Locate every blood parasite and identify its species.
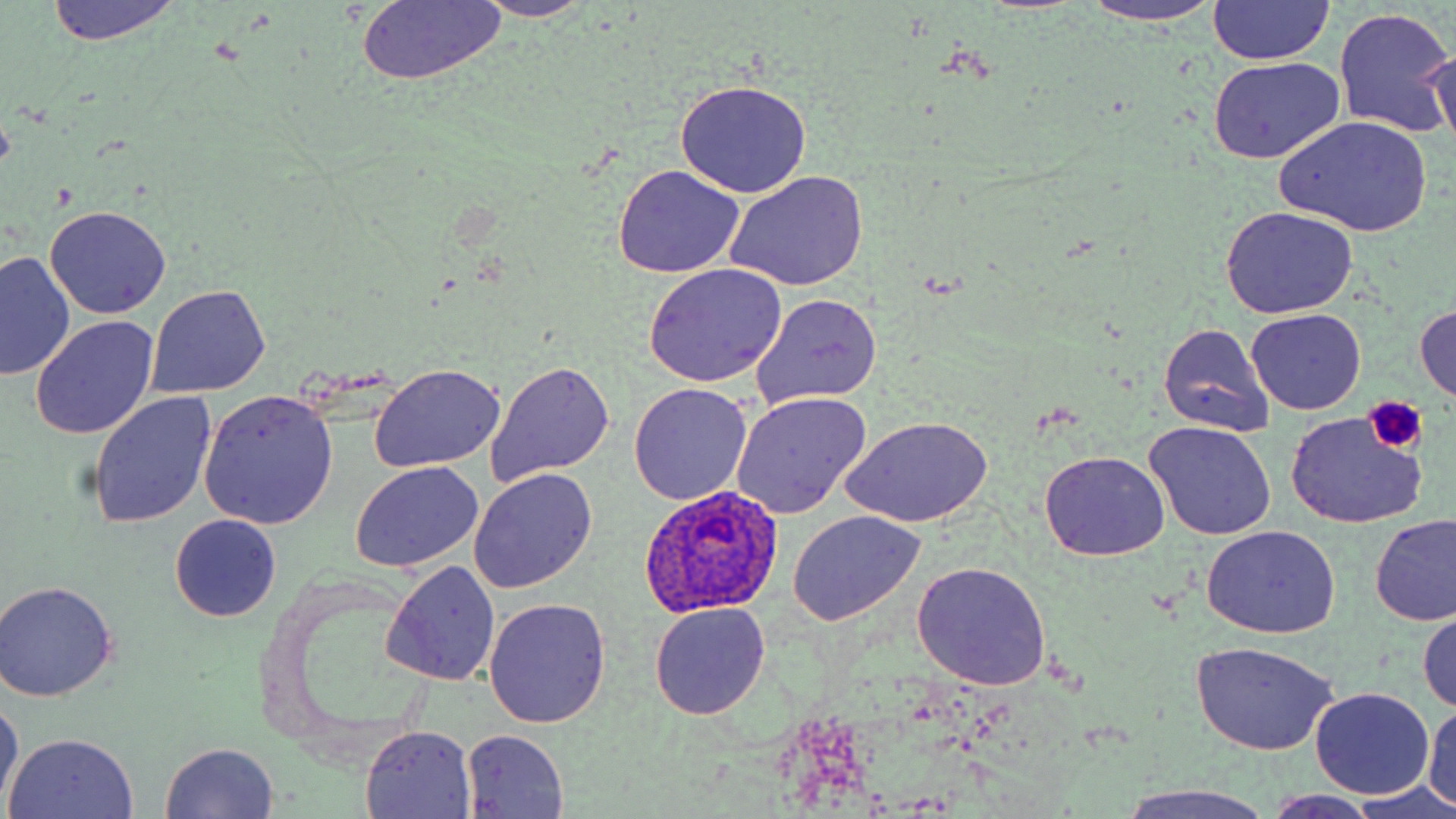
Approximate bounding boxes as [x1, y1, x2, y2] in pixels.
Plasmodium ovale-infected red blood cells: [638, 486, 785, 617].
No Plasmodium falciparum, Plasmodium malariae, Plasmodium vivax, Babesia divergens, or Trypanosoma brucei observed.

Summary:
  - Uninfected red blood cell locations: [45, 0, 182, 45], [356, 0, 505, 86], [472, 0, 595, 21], [1207, 0, 1335, 67], [1083, 2, 1229, 26], [1335, 8, 1455, 137], [1425, 47, 1454, 155], [1208, 56, 1345, 163], [673, 80, 812, 197], [1275, 116, 1432, 237], [614, 165, 745, 278], [724, 171, 870, 292], [44, 206, 172, 320], [1220, 207, 1359, 318], [0, 251, 74, 381], [644, 265, 789, 386], [148, 286, 270, 399], [752, 292, 882, 409], [1414, 304, 1456, 402], [1246, 308, 1365, 414], [30, 316, 160, 439], [1159, 325, 1274, 437], [49, 344, 204, 487], [488, 360, 615, 483], [369, 364, 506, 472], [630, 384, 752, 505], [86, 391, 217, 529], [198, 391, 337, 528], [732, 392, 872, 518], [840, 415, 993, 528], [1285, 415, 1424, 529], [1142, 422, 1277, 542], [1039, 451, 1169, 562], [351, 462, 484, 572], [470, 468, 598, 594], [787, 512, 923, 624], [169, 515, 282, 621], [1370, 515, 1456, 625], [1201, 526, 1339, 640], [382, 561, 500, 688], [911, 561, 1053, 688], [0, 580, 119, 700], [484, 600, 609, 727], [649, 601, 771, 720], [1419, 614, 1456, 715], [1190, 641, 1340, 755], [1311, 689, 1434, 799], [0, 697, 23, 810], [1425, 702, 1456, 807], [362, 726, 476, 816], [460, 730, 569, 817], [5, 733, 139, 819], [158, 742, 281, 818], [1112, 784, 1277, 819], [1343, 784, 1456, 817], [1263, 791, 1388, 817]
  - Platelet locations: [1364, 396, 1425, 451]
  - Slide-level diagnosis: Plasmodium ovale
  - Image size: 1456×819 pixels
  - Stain: May-Grünwald-Giemsa
  - Field of view: single
  - Magnification: 1000x
  - Preparation: thin blood film
  - Modality: optical microscopy